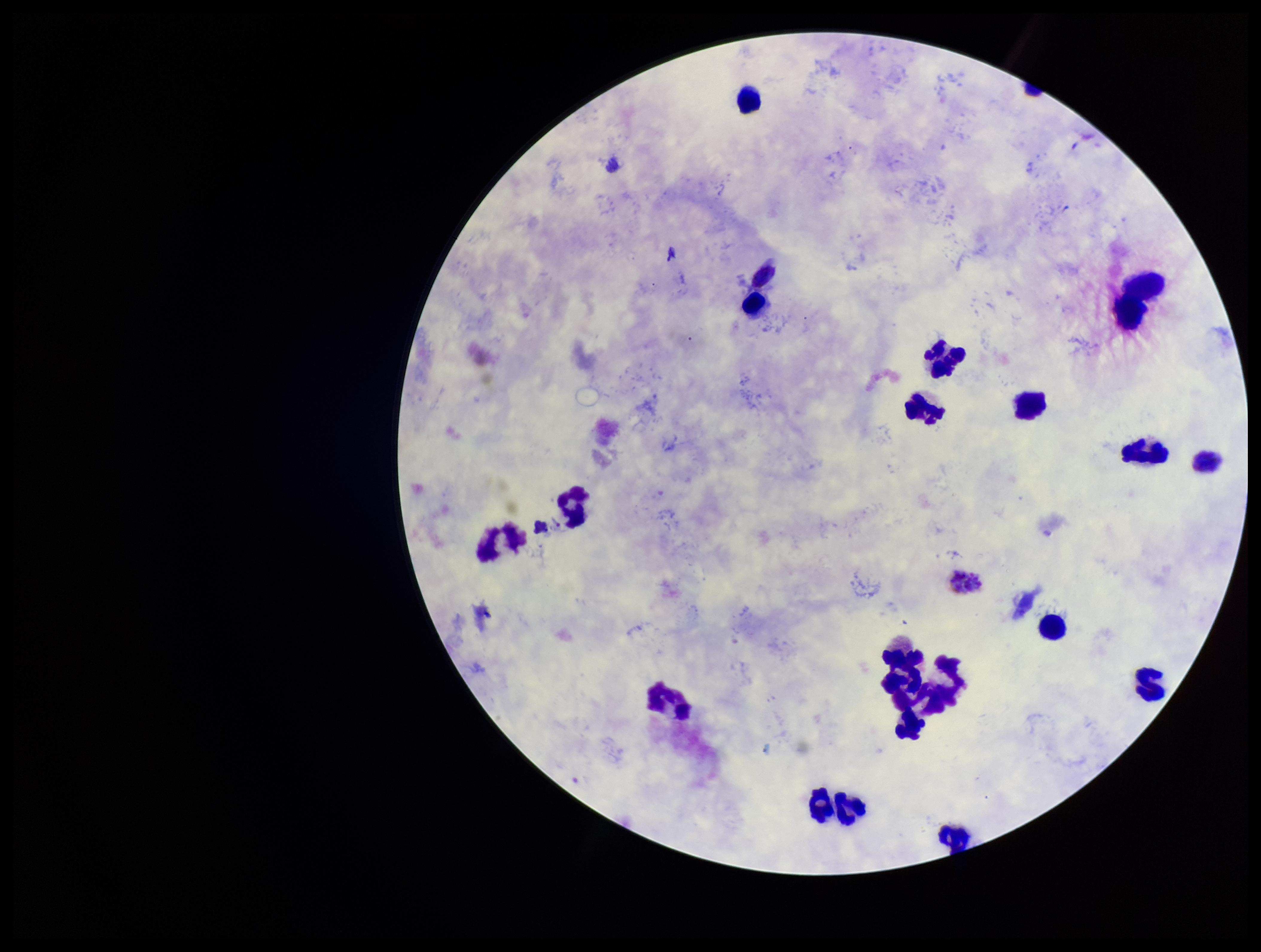

{
  "leukocyte_count": 22,
  "patient_malaria_status": "positive",
  "capture": "smartphone photograph through the microscope eyepiece",
  "plasmodium_parasites": "none seen",
  "preparation": "thick blood smear",
  "parasite_count": 0,
  "stain": "Giemsa",
  "species_reported_for_this_patient": "Plasmodium vivax",
  "field_of_view": "single",
  "image_size": "1261×952 pixels"
}